State which parasite is depicted.
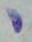
Toxoplasma gondii.

Summary:
  - Magnification: 1000x
  - Modality: photomicrograph